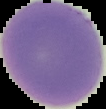 Malaria status: uninfected. From a thin blood smear. The area outside the segmented cell region is set to black. Image is 106×109 pixels.